Give the position of every Plasmodium parasite.
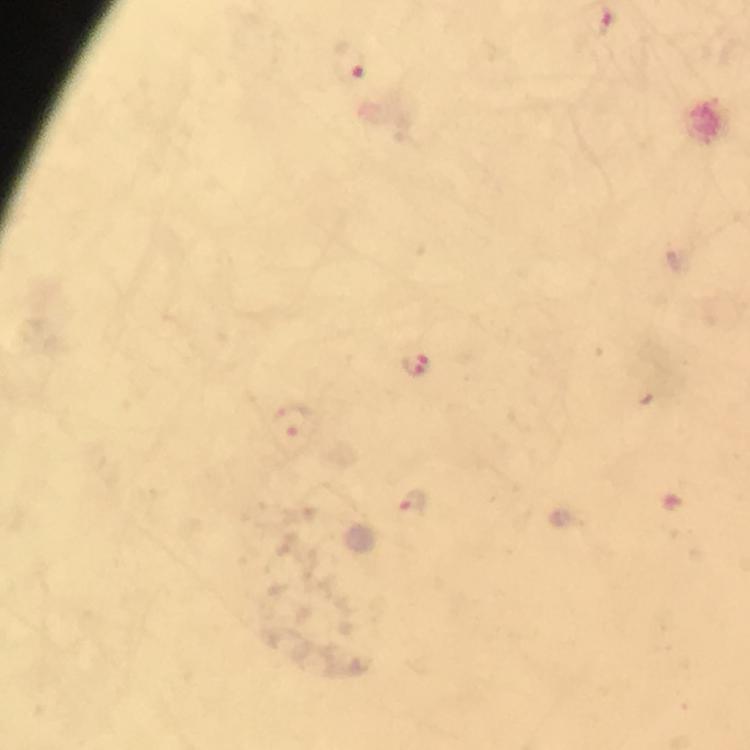
Approximate centers as (x, y) in pixels.
Plasmodium parasites: (351, 64), (415, 363), (289, 418), (413, 504).

Thick smear. From a diagnostic examination for malaria. Immersion oil was used. Photographed with a smartphone mounted on the microscope. Image is 750×750 pixels. At 100x magnification. Giemsa stain. Cropped region of a single field of view.